Report the malaria status of this cell.
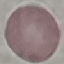

It is uninfected.

Summary:
  - Capture: smartphone camera at the microscope eyepiece
  - Image type: automatically extracted cell patch, resized to 64 × 64 pixels
  - Stain: Giemsa
  - Preparation: thin smear